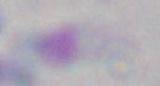

Summary:
  - Magnification: 1000x
  - Modality: photomicrograph
  - Identification: Toxoplasma gondii